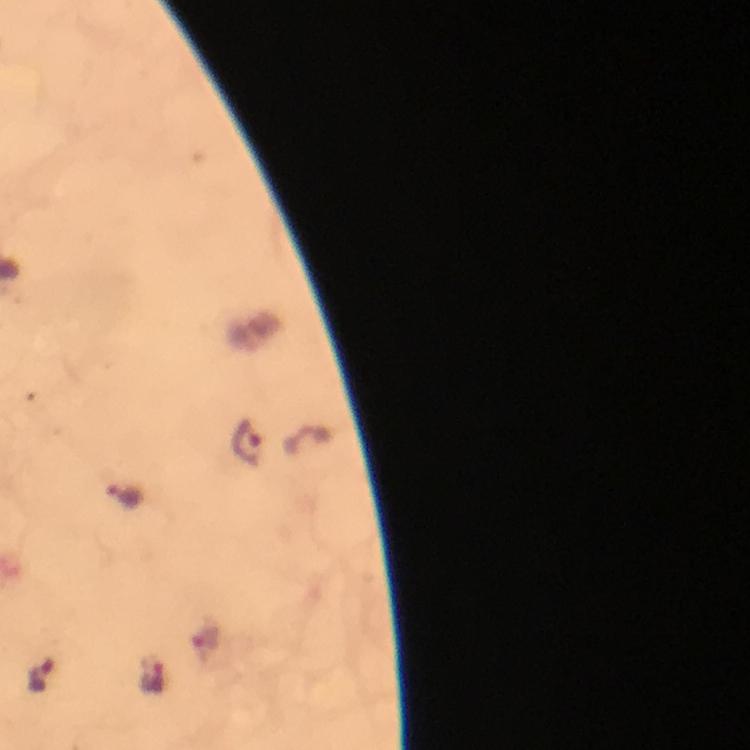

Approximate centers as [x, y] in pixels. Malaria parasite locations: [247, 444], [124, 496], [43, 674], [154, 678]. A crop from one field of view. From a diagnostic examination for malaria. Smartphone photograph taken through a microscope. Thick blood film. Giemsa-stained preparation. Immersion oil applied. At 100x magnification. Image is 750×750 pixels.